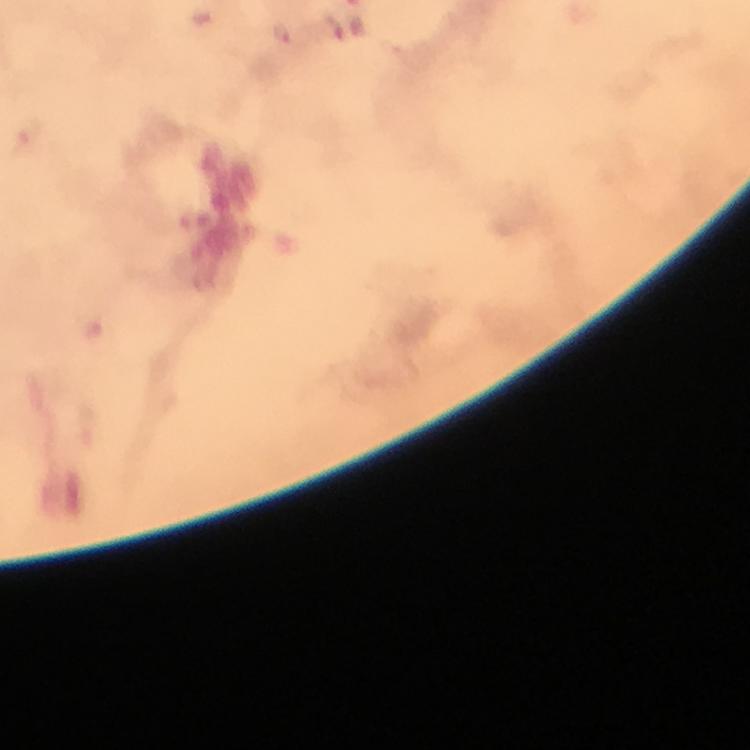

Approximate centers as (x, y) in pixels.
Summary:
  - Plasmodium parasite locations: (282, 33)
  - Stain: Giemsa
  - Immersion oil: used
  - Capture: smartphone photograph through a microscope
  - Image size: 750×750 pixels
  - Magnification: 100x
  - Preparation: thick smear
  - Context: from a malaria diagnostic workup
  - Cropped from: one field of view